Locate every blood parasite and identify its species.
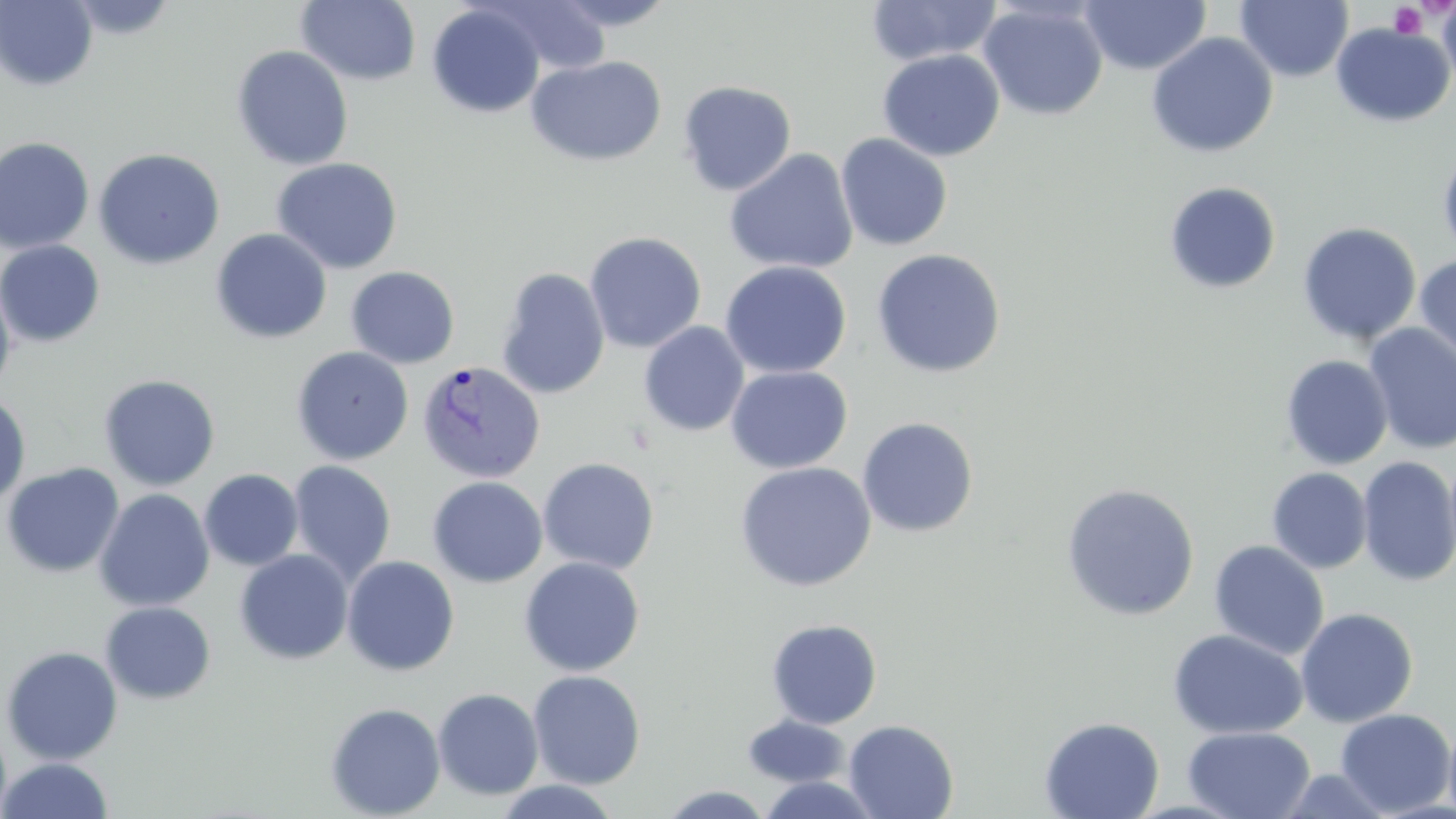
Approximate bounding boxes as (x1,y1)-(x2,y2) corner pairs in pixels.
Plasmodium vivax-infected red blood cells: (417,361)-(545,485).
No Plasmodium falciparum, Plasmodium ovale, Plasmodium malariae, Babesia divergens, or Trypanosoma brucei observed.

slide-level diagnosis = Plasmodium vivax
image size = 1456×819 pixels
field of view = one of a larger specimen
stain = May-Grünwald-Giemsa
preparation = thin blood smear
uninfected red blood cell locations = approximate bounding boxes as (x1,y1)-(x2,y2) corner pairs in pixels: (295,0)-(422,86), (483,0)-(612,76), (865,0)-(1002,66), (1079,0)-(1211,75), (1236,0)-(1353,82), (1437,0)-(1456,89), (1,1)-(98,90), (543,1)-(682,31), (978,2)-(1108,120), (427,4)-(545,117), (1330,23)-(1455,128), (1146,32)-(1278,158), (231,45)-(354,171), (877,49)-(1005,161), (526,55)-(668,167), (677,80)-(797,196), (835,133)-(953,251), (0,136)-(95,254), (1438,145)-(1456,263), (93,148)-(226,270), (724,148)-(858,275), (271,157)-(403,274), (1163,181)-(1282,295), (1297,222)-(1421,345), (210,228)-(332,344), (584,231)-(707,353), (0,240)-(105,347), (871,248)-(1006,378), (1414,253)-(1456,369), (720,261)-(851,379), (346,266)-(460,368), (495,267)-(610,399), (0,278)-(17,400), (639,321)-(750,437), (1363,323)-(1456,455), (291,346)-(413,465), (1280,354)-(1393,469), (725,365)-(853,474), (98,374)-(221,491), (0,394)-(31,507), (857,417)-(979,538), (1357,456)-(1456,587), (538,457)-(659,574), (288,460)-(396,584), (735,461)-(877,592), (1,462)-(124,578), (1267,467)-(1373,574), (199,469)-(303,571), (427,476)-(548,588), (1060,482)-(1200,621), (94,488)-(214,612), (1209,540)-(1329,660), (234,549)-(354,665), (341,555)-(460,676), (519,557)-(645,677), (100,601)-(216,704), (1295,607)-(1419,727), (766,618)-(882,729), (1168,628)-(1308,739), (1,645)-(123,764), (528,670)-(645,789), (432,688)-(544,800), (324,702)-(446,819), (1334,708)-(1456,816), (1444,712)-(1456,819), (742,715)-(851,788), (1039,716)-(1165,819), (0,719)-(11,819), (843,719)-(958,818), (1183,726)-(1316,819), (1,757)-(114,818), (755,774)-(885,818), (493,780)-(623,818), (657,785)-(776,818)
platelet locations = approximate bounding boxes as (x1,y1)-(x2,y2) corner pairs in pixels: (1388,3)-(1427,39)
magnification = 1000x
modality = light microscopy